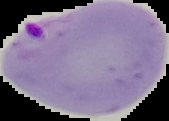
Segmented cell region on a black background. From a thin blood film. Image is 169×121 pixels. Result: malaria parasites detected.